Name the blood parasite species.
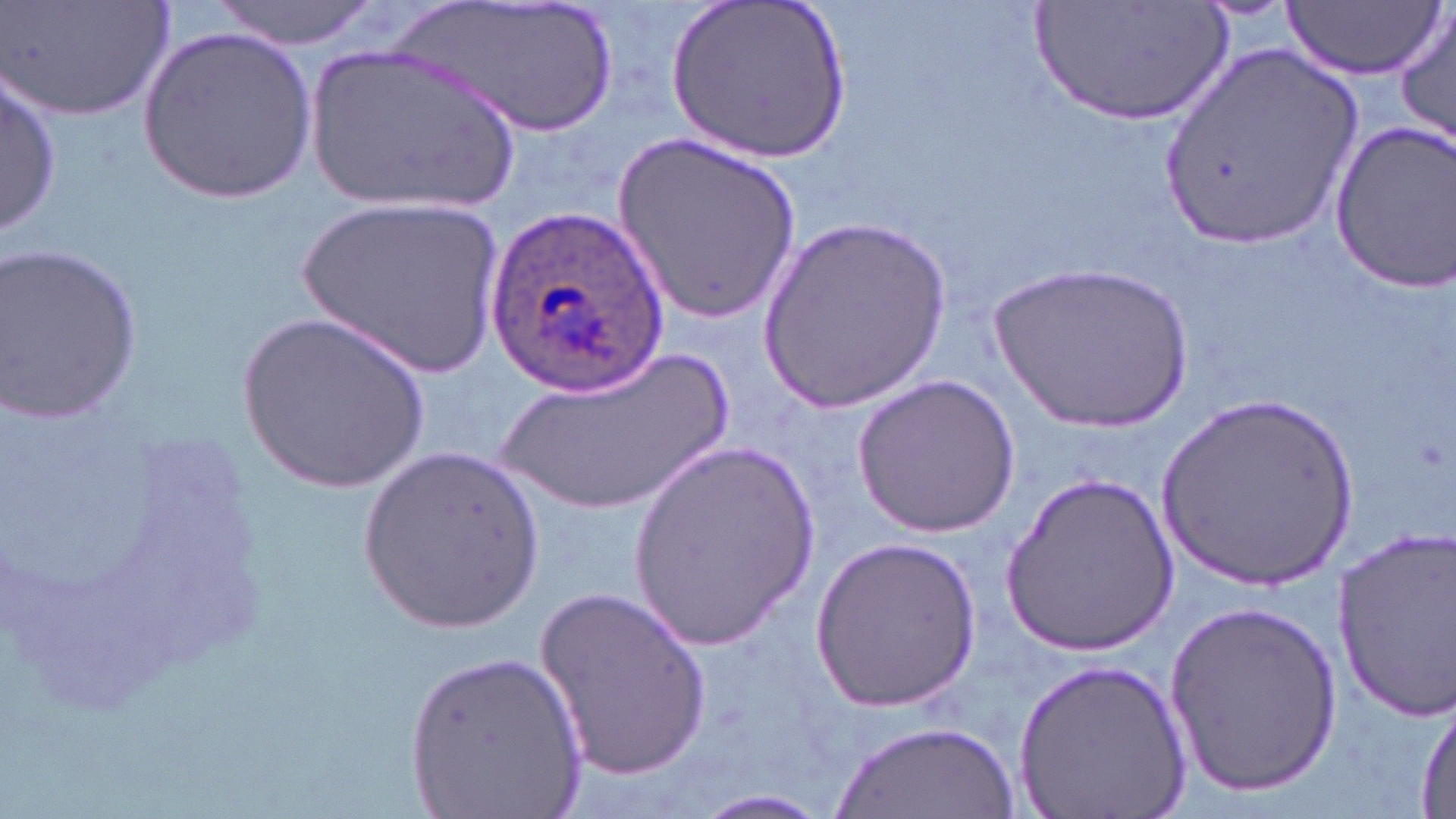

Plasmodium ovale.

Summary:
  - Coordinate format: approximate bounding boxes as [x1, y1, x2, y2] in pixels
  - Plasmodium ovale-infected red blood cell locations: [484, 206, 667, 397]
  - Uninfected red blood cell locations: [3, 0, 172, 122], [210, 0, 384, 49], [399, 0, 626, 138], [666, 0, 850, 165], [1035, 3, 1231, 128], [1282, 3, 1444, 80], [1393, 5, 1455, 151], [140, 24, 316, 199], [303, 40, 524, 216], [1155, 44, 1365, 251], [1, 71, 60, 237], [1328, 122, 1456, 289], [610, 132, 801, 325], [302, 196, 507, 382], [757, 217, 951, 416], [2, 246, 146, 420], [989, 259, 1195, 436], [235, 309, 431, 494], [484, 347, 749, 521], [853, 374, 1022, 536], [1156, 397, 1358, 596], [625, 439, 819, 651], [362, 448, 545, 633], [999, 471, 1179, 657], [1329, 523, 1456, 715], [807, 537, 986, 710], [539, 584, 711, 780], [1163, 598, 1343, 792], [405, 650, 589, 819], [1013, 655, 1192, 819], [1413, 695, 1455, 816], [833, 720, 1018, 818], [692, 790, 833, 818]
  - Image size: 1456×819 pixels
  - Preparation: thin blood film
  - Field of view: single
  - Stain: May-Grünwald-Giemsa
  - Magnification: 1000x
  - Modality: light microscopy